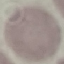
{
  "result": "negative for malaria parasites",
  "image_type": "automatically extracted cell patch, resized to 64 × 64 pixels",
  "preparation": "thin blood film",
  "stain": "Giemsa",
  "capture": "smartphone camera at the microscope eyepiece"
}